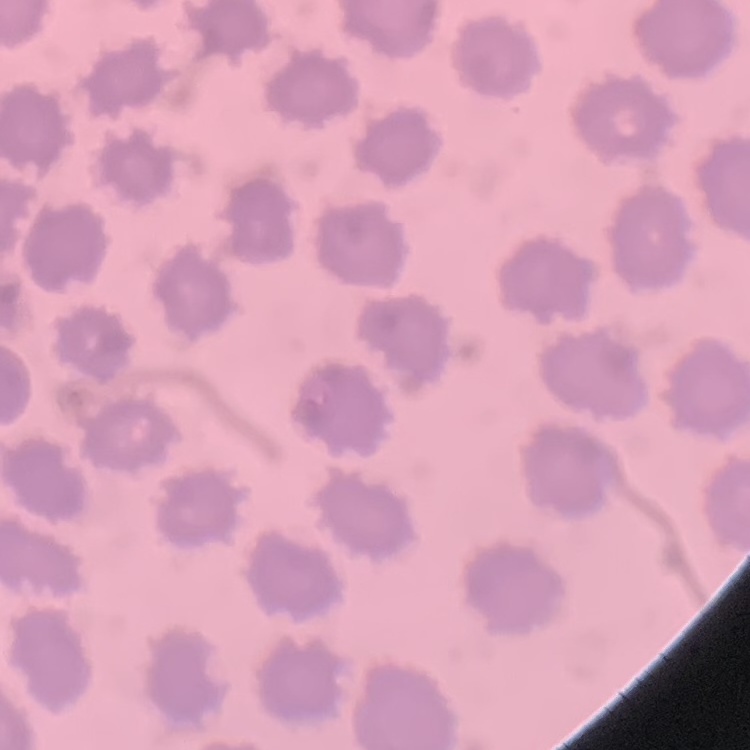

{
  "erythrocyte_morphology": "no rouleaux formation",
  "image_type": "one tile cut from a larger photomicrograph",
  "stain": "Field's or Giemsa",
  "preparation": "thin blood film"
}